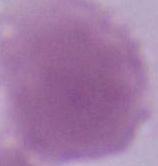

modality = micrograph
magnification = 1000x
identification = erythrocyte